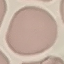
Malaria status: uninfected. Thin blood film. Giemsa stain. Photographed with a smartphone camera at the microscope eyepiece. Automatically extracted cell patch, resized to 64 × 64 pixels.